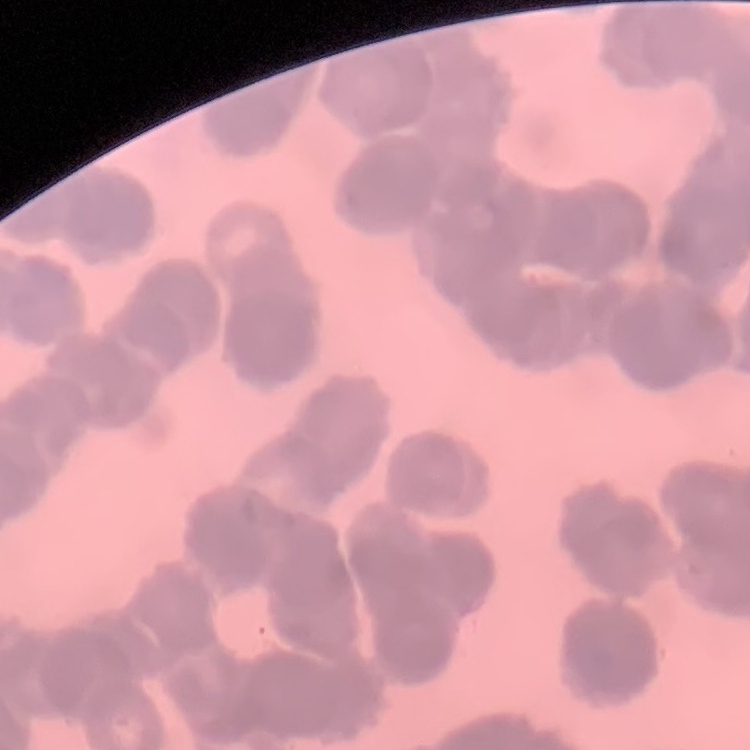
The red blood cells show rouleaux formation. Thin peripheral smear. Field's or Giemsa stain. Square crop of a larger photomicrograph.